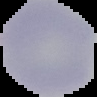

image_type: segmented cell region on a black background
image_size: 97×97 pixels
preparation: thin blood smear
malaria_status: uninfected